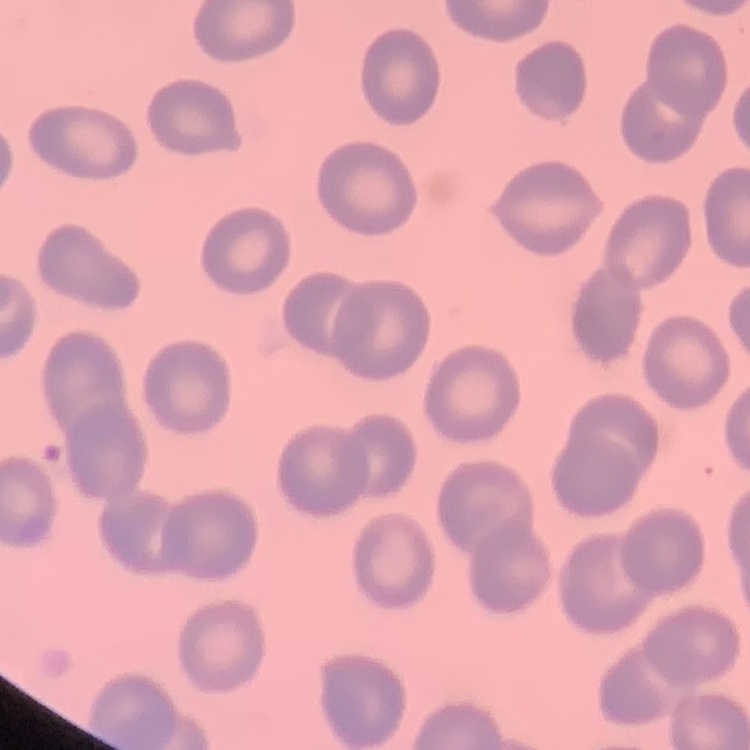

Summary:
  - Red blood cell morphology: no rouleaux formation
  - Preparation: thin blood smear
  - Image type: one tile cut from a larger photomicrograph
  - Stain: Field's or Giemsa